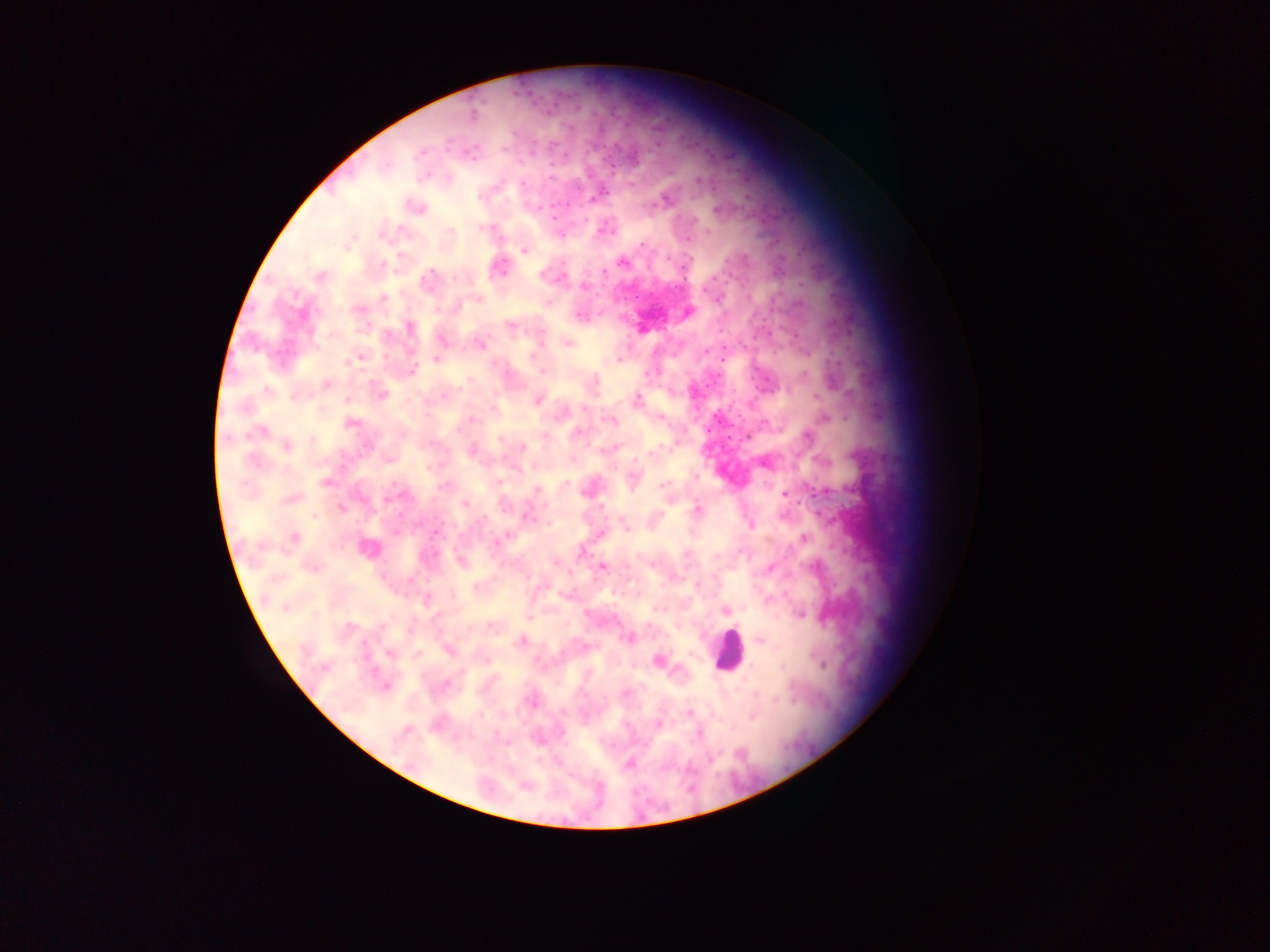 Approximate centers as (x, y) in pixels. Leukocyte locations: (729, 651). Malaria parasite locations: (473, 113), (503, 149), (420, 153), (471, 154), (552, 177), (449, 179), (522, 183), (631, 183), (599, 195), (665, 200), (536, 207), (418, 208), (716, 209), (553, 216), (584, 220), (692, 220), (482, 228), (401, 229), (451, 231), (605, 231), (707, 231), (560, 235), (688, 239), (347, 244), (641, 245), (523, 250), (622, 263), (562, 264), (384, 265), (500, 267), (604, 272), (320, 277), (456, 278), (428, 279), (585, 287), (679, 289), (383, 299), (718, 300), (548, 302), (360, 310), (579, 316), (510, 325), (410, 328), (442, 340), (568, 343), (480, 344), (705, 351), (361, 356), (437, 358), (534, 358), (620, 360), (346, 361), (412, 371), (541, 372), (648, 373), (804, 375), (596, 381), (327, 385), (267, 391), (381, 394), (443, 396), (296, 397), (537, 400), (636, 401), (825, 419), (473, 420), (610, 420), (350, 422), (458, 429), (261, 431), (545, 436), (808, 437), (287, 446), (523, 446), (471, 450), (603, 450), (651, 454), (389, 460), (255, 461), (697, 476), (633, 479), (326, 482), (567, 484), (445, 485), (662, 485), (536, 490), (785, 494), (291, 499), (387, 499), (464, 505), (341, 508), (698, 510), (315, 516), (526, 516), (484, 518), (549, 524), (623, 524), (750, 525), (437, 531), (397, 532), (601, 534), (805, 537), (294, 538), (496, 544), (367, 549), (581, 553), (685, 555), (463, 561), (602, 567), (313, 569), (769, 569), (696, 586), (427, 600), (285, 607), (725, 611), (799, 614), (349, 626), (649, 626), (492, 627), (628, 638), (759, 641), (521, 642), (449, 651), (389, 653), (540, 661), (658, 661), (324, 668), (445, 686), (386, 687), (625, 693), (531, 701), (688, 714), (658, 723), (405, 732), (562, 733), (699, 734), (630, 763), (525, 785). One field of view. Thick blood film. Collected in Ghana. Photographed through a microscope with a mobile-phone camera. Image is 1270×952 pixels.